Identify the blood parasite species.
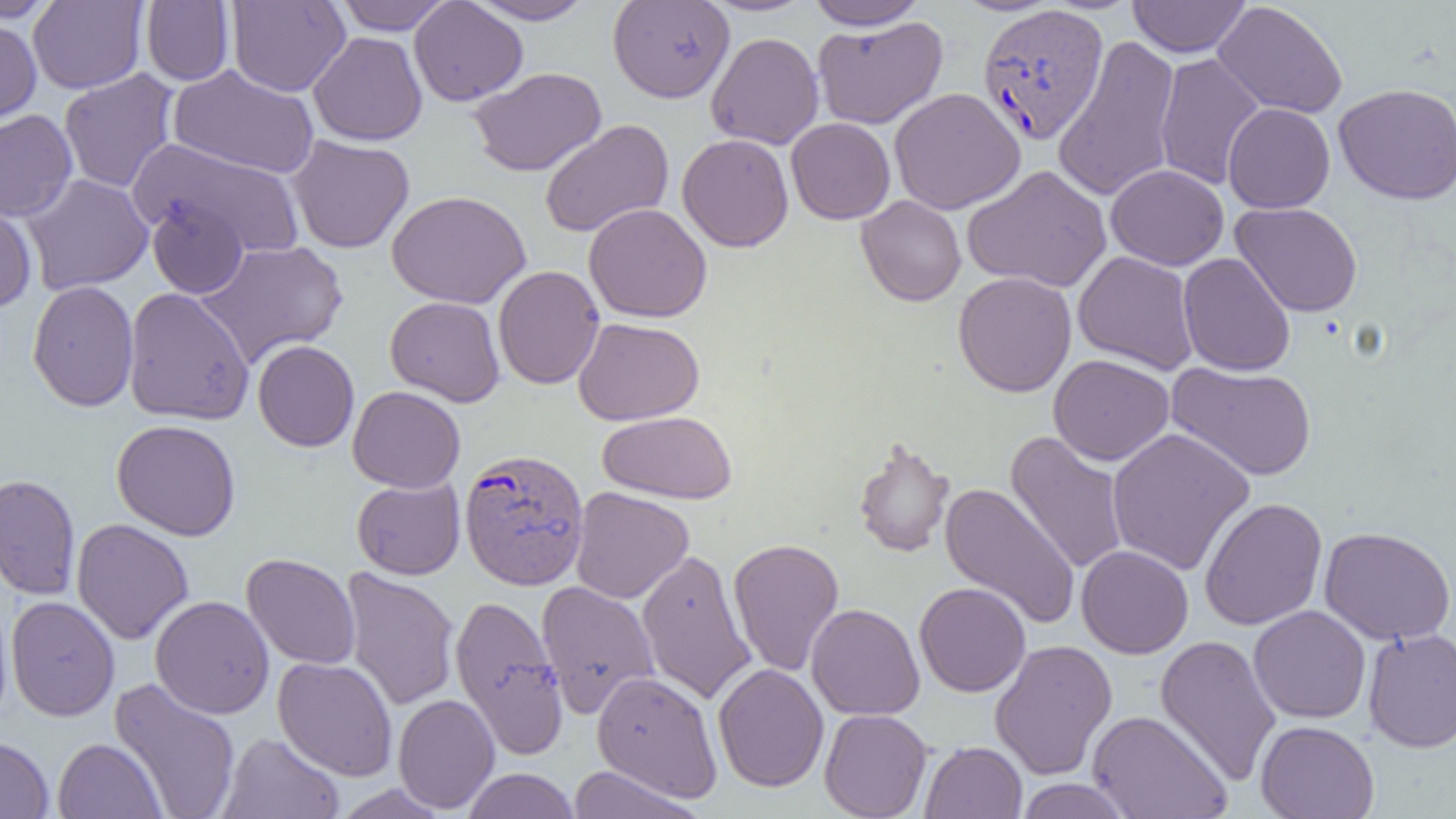

Plasmodium vivax.

uninfected red blood cell locations = approximate bounding boxes as named x1/y1/x2/y2 corners in pixels: (x1=0, y1=0, x2=61, y2=23), (x1=333, y1=0, x2=453, y2=35), (x1=409, y1=0, x2=528, y2=106), (x1=464, y1=0, x2=598, y2=25), (x1=608, y1=0, x2=734, y2=102), (x1=701, y1=0, x2=818, y2=16), (x1=1128, y1=0, x2=1251, y2=57), (x1=28, y1=1, x2=147, y2=94), (x1=141, y1=1, x2=235, y2=85), (x1=227, y1=1, x2=350, y2=97), (x1=805, y1=1, x2=930, y2=30), (x1=1213, y1=1, x2=1348, y2=118), (x1=812, y1=16, x2=948, y2=130), (x1=0, y1=17, x2=42, y2=128), (x1=308, y1=31, x2=427, y2=146), (x1=705, y1=32, x2=824, y2=149), (x1=1052, y1=35, x2=1182, y2=203), (x1=1154, y1=53, x2=1266, y2=191), (x1=168, y1=65, x2=320, y2=179), (x1=469, y1=67, x2=607, y2=177), (x1=58, y1=68, x2=179, y2=193), (x1=1333, y1=83, x2=1456, y2=205), (x1=889, y1=87, x2=1025, y2=214), (x1=1223, y1=103, x2=1335, y2=213), (x1=0, y1=110, x2=77, y2=222), (x1=786, y1=118, x2=895, y2=224), (x1=539, y1=119, x2=674, y2=238), (x1=677, y1=133, x2=794, y2=252), (x1=286, y1=135, x2=415, y2=253), (x1=130, y1=139, x2=306, y2=259), (x1=962, y1=164, x2=1112, y2=293), (x1=1106, y1=164, x2=1229, y2=270), (x1=21, y1=173, x2=154, y2=295), (x1=387, y1=190, x2=531, y2=309), (x1=856, y1=195, x2=966, y2=306), (x1=147, y1=197, x2=248, y2=299), (x1=0, y1=202, x2=37, y2=311), (x1=1230, y1=202, x2=1363, y2=317), (x1=584, y1=203, x2=712, y2=323), (x1=195, y1=239, x2=348, y2=368), (x1=1073, y1=250, x2=1199, y2=375), (x1=1178, y1=252, x2=1295, y2=377), (x1=493, y1=265, x2=605, y2=390), (x1=952, y1=271, x2=1077, y2=397), (x1=27, y1=280, x2=139, y2=411), (x1=123, y1=287, x2=255, y2=425), (x1=385, y1=296, x2=505, y2=407), (x1=573, y1=317, x2=705, y2=425), (x1=252, y1=339, x2=359, y2=452), (x1=1049, y1=354, x2=1174, y2=465), (x1=1165, y1=361, x2=1316, y2=480), (x1=348, y1=385, x2=466, y2=492), (x1=597, y1=410, x2=738, y2=504), (x1=111, y1=419, x2=241, y2=541), (x1=1106, y1=427, x2=1256, y2=576), (x1=1005, y1=429, x2=1129, y2=575), (x1=853, y1=436, x2=956, y2=558), (x1=0, y1=474, x2=81, y2=600), (x1=351, y1=476, x2=465, y2=580), (x1=940, y1=482, x2=1080, y2=630), (x1=570, y1=487, x2=694, y2=604), (x1=1199, y1=497, x2=1328, y2=630), (x1=72, y1=518, x2=193, y2=645), (x1=1319, y1=526, x2=1455, y2=645), (x1=728, y1=537, x2=844, y2=677), (x1=1076, y1=545, x2=1194, y2=659), (x1=636, y1=548, x2=757, y2=705), (x1=241, y1=553, x2=360, y2=670), (x1=340, y1=567, x2=460, y2=712), (x1=536, y1=580, x2=660, y2=719), (x1=914, y1=581, x2=1031, y2=697), (x1=449, y1=594, x2=567, y2=759), (x1=150, y1=595, x2=275, y2=719), (x1=6, y1=596, x2=120, y2=722), (x1=806, y1=603, x2=925, y2=720), (x1=1248, y1=605, x2=1371, y2=724), (x1=1363, y1=627, x2=1456, y2=753), (x1=1155, y1=634, x2=1281, y2=785), (x1=989, y1=639, x2=1118, y2=779), (x1=273, y1=656, x2=398, y2=781), (x1=713, y1=663, x2=829, y2=792), (x1=592, y1=670, x2=723, y2=802), (x1=109, y1=677, x2=242, y2=819), (x1=393, y1=693, x2=500, y2=813), (x1=819, y1=709, x2=933, y2=819), (x1=1087, y1=709, x2=1233, y2=819), (x1=1255, y1=720, x2=1380, y2=818), (x1=218, y1=731, x2=344, y2=819), (x1=0, y1=735, x2=54, y2=819), (x1=53, y1=737, x2=166, y2=818), (x1=920, y1=741, x2=1027, y2=818), (x1=567, y1=765, x2=708, y2=818), (x1=462, y1=768, x2=580, y2=819), (x1=1014, y1=778, x2=1133, y2=818), (x1=330, y1=783, x2=451, y2=818)
Plasmodium vivax-infected red blood cell locations = approximate bounding boxes as named x1/y1/x2/y2 corners in pixels: (x1=978, y1=4, x2=1109, y2=144), (x1=459, y1=449, x2=590, y2=591)
modality = light microscopy
image size = 1456×819 pixels
preparation = thin blood film
field of view = single
magnification = 1000x